Report the malaria status of this cell.
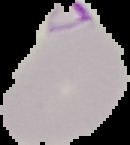
Parasitized.

image size = 130×145 pixels
image type = segmented cell region on a black background
preparation = thin blood smear